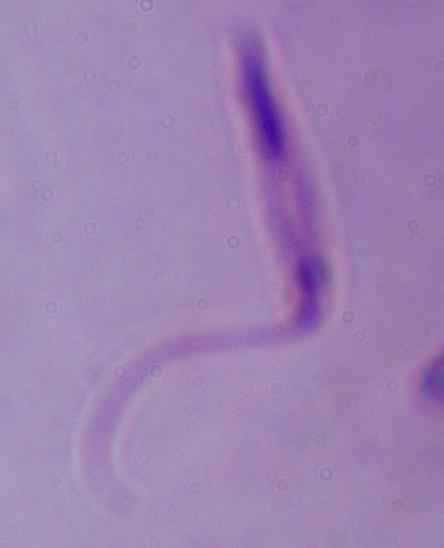
Summary:
  - Modality: photomicrograph
  - Identification: Leishmania
  - Magnification: 1000x